Classify this cell by malaria status.
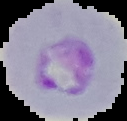

It is parasitized.

Summary:
  - Image size: 127×121 pixels
  - Image type: segmented cell region with the area outside set to black
  - Preparation: thin blood film